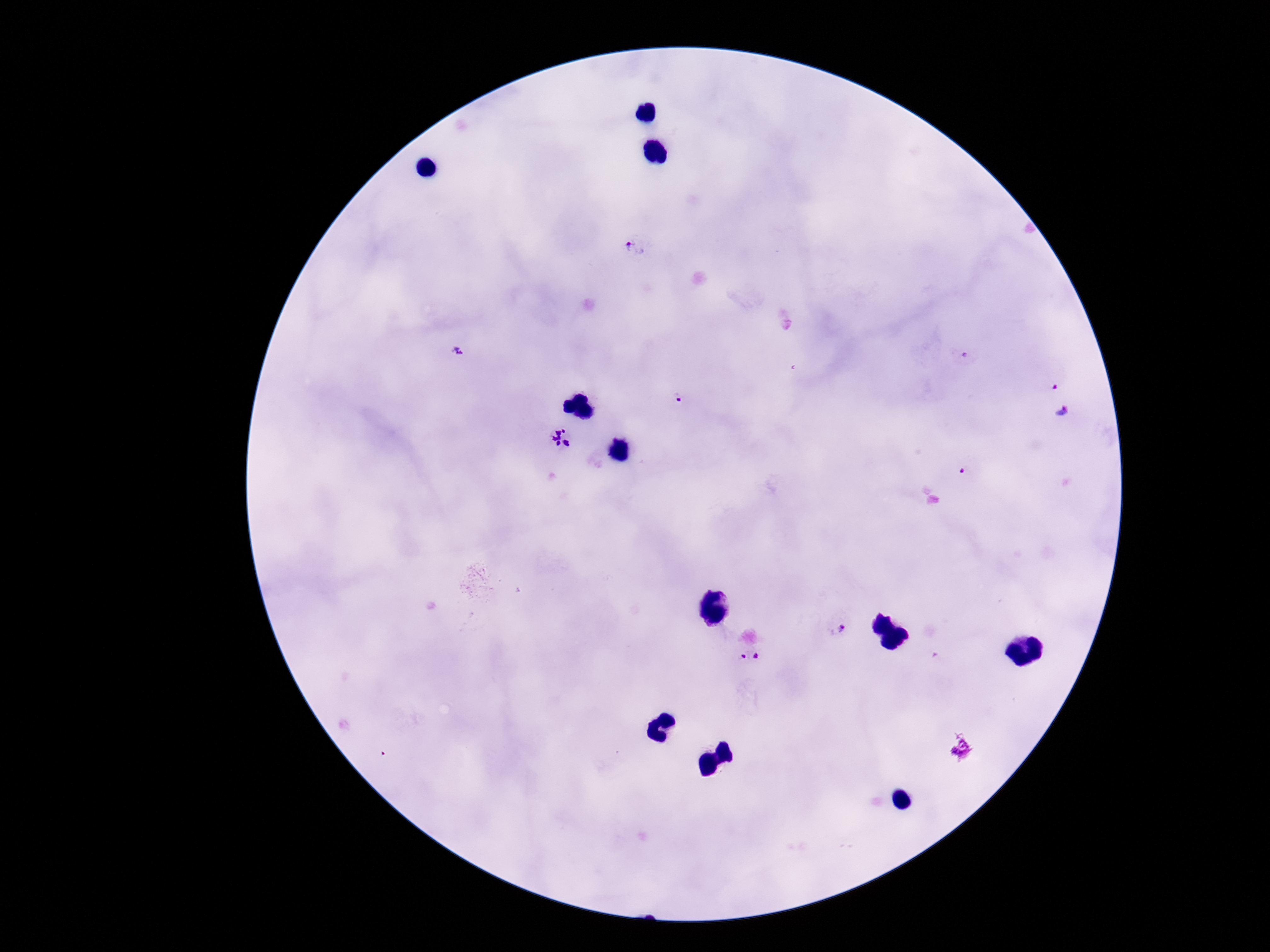

Approximate centers as {x, y} in pixels.
Summary:
  - Plasmodium parasite locations: {636, 246}, {457, 350}, {1054, 385}, {679, 398}, {1063, 410}, {559, 438}, {962, 472}, {836, 627}, {749, 659}
  - Stain: Giemsa
  - Magnification: 100x
  - Image size: 1270×952 pixels
  - Field of view: single
  - Preparation: thick blood film
  - Capture: smartphone camera through the microscope eyepiece
  - Patient malaria status: positive